Assess the morphology of the erythrocytes.
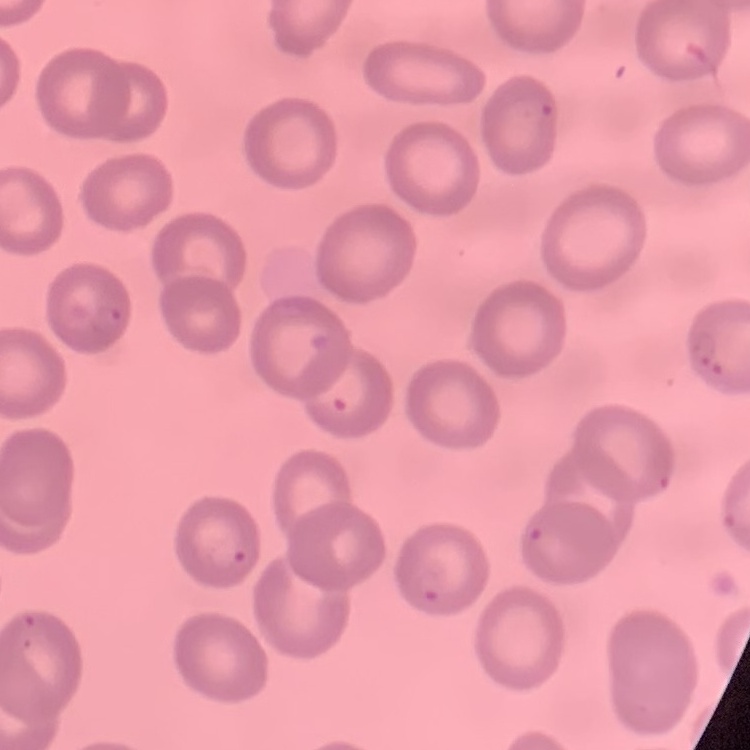

They show no rouleaux formation.

Summary:
  - Stain: Field's or Giemsa
  - Preparation: thin blood smear
  - Image type: square crop of a larger photomicrograph